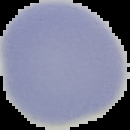

preparation = thin blood film
image size = 130×130 pixels
image type = segmented cell region on a black background
result = no malaria parasites seen